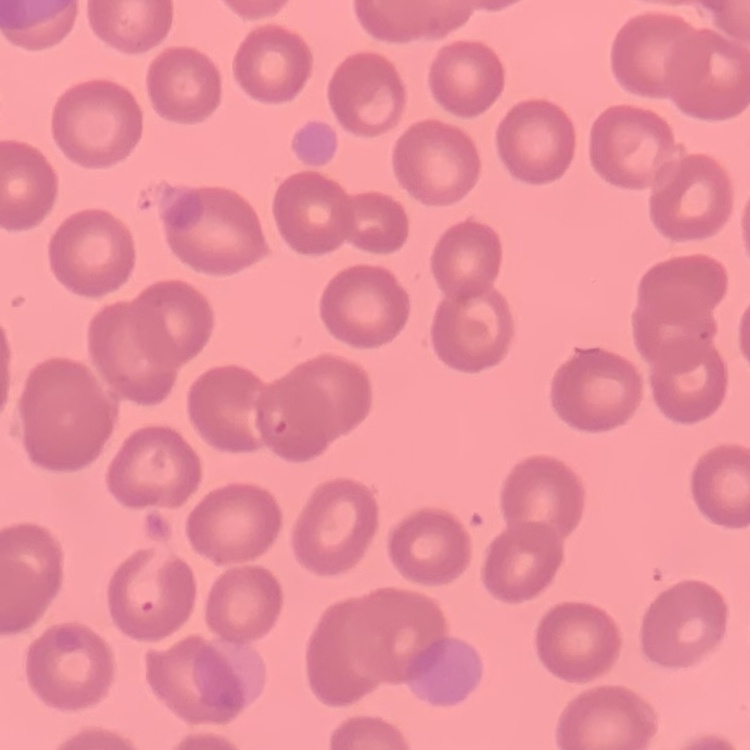
red_blood_cell_morphology: no rouleaux formation
image_type: square crop of a larger photomicrograph
stain: Field's or Giemsa
preparation: thin blood smear